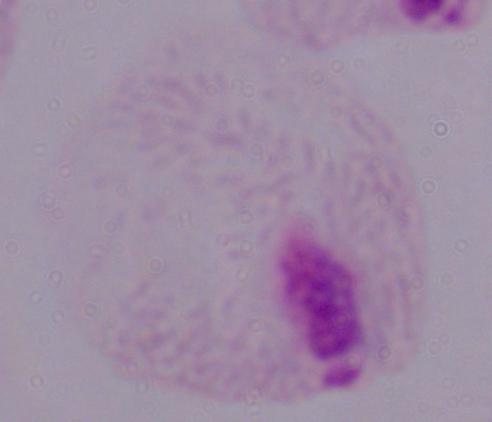
Summary:
  - Identification: trichomonad
  - Magnification: 1000x
  - Modality: photomicrograph